Identify the parasite.
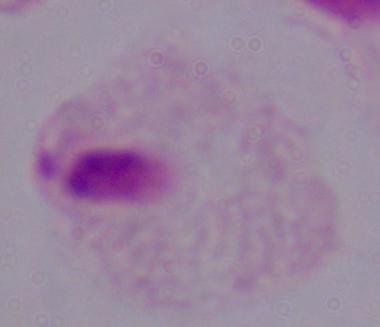
A trichomonad.

{
  "magnification": "1000x",
  "modality": "photomicrograph"
}